Point out every malaria parasite and every leukocyte.
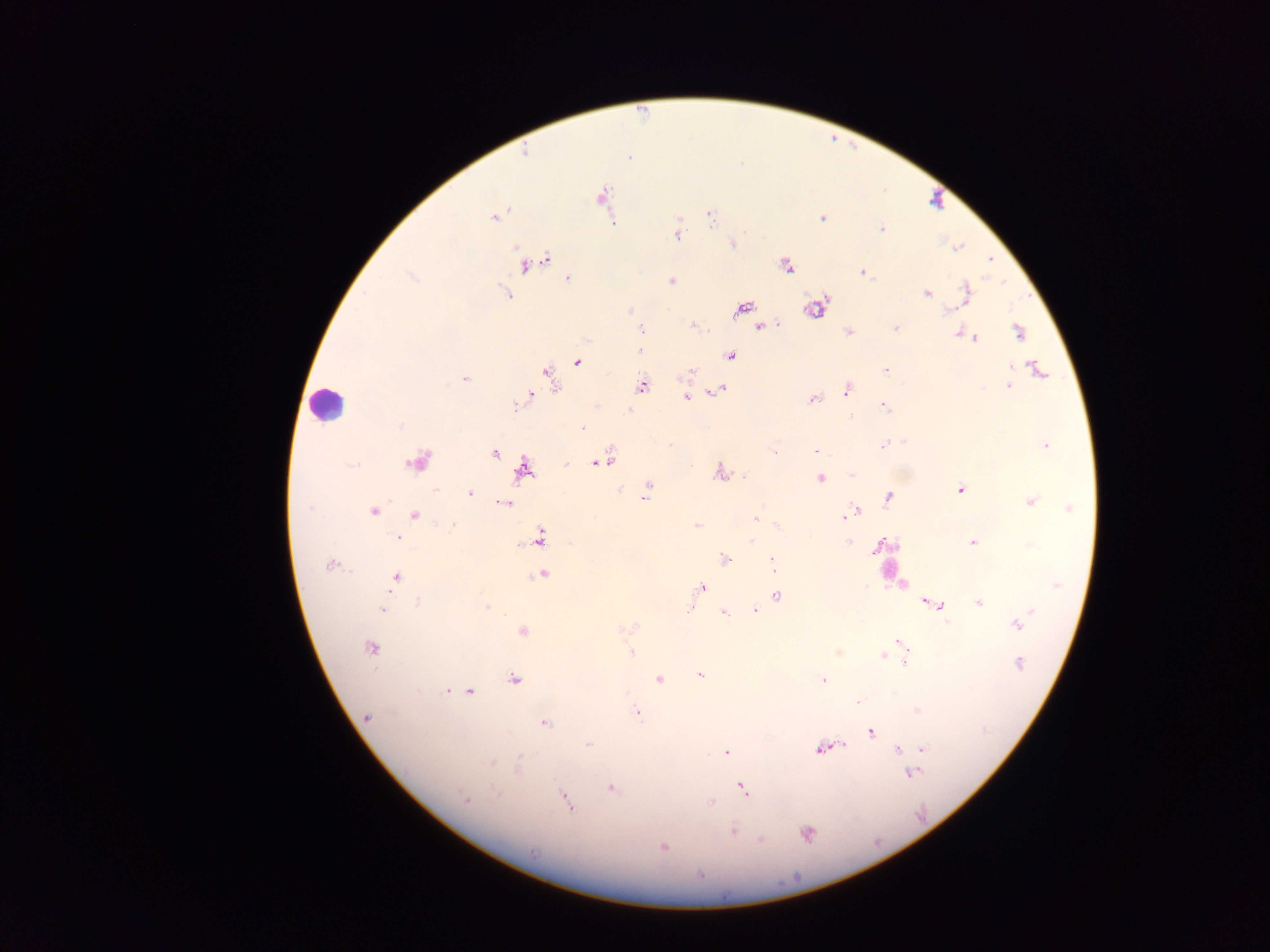

Approximate centers as (x, y) in pixels.
Malaria parasites: (629, 157), (602, 198), (494, 216), (710, 216), (822, 218), (613, 222), (882, 228), (677, 233), (732, 244), (959, 246), (991, 259), (533, 262), (786, 266), (863, 273), (410, 275), (568, 279), (671, 280), (967, 293), (507, 294), (927, 294), (815, 308), (742, 309), (629, 310), (950, 311), (693, 326), (760, 327), (896, 328), (641, 329), (848, 332), (1018, 332), (958, 334), (975, 338), (640, 350), (730, 356), (578, 362), (1037, 368), (885, 370), (690, 372), (548, 375), (464, 379), (641, 386), (1008, 386), (720, 389), (847, 389), (527, 397), (686, 397), (813, 399), (519, 403), (884, 405), (630, 411), (400, 426), (583, 428), (669, 445), (882, 445), (1046, 446), (816, 450), (495, 453), (775, 453), (417, 462), (601, 462), (566, 464), (524, 470), (719, 472), (744, 476), (851, 476), (821, 478), (649, 486), (960, 490), (470, 493), (646, 497), (889, 497), (1030, 502), (505, 503), (309, 507), (1069, 509), (374, 512), (858, 512), (851, 515), (415, 516), (844, 517), (755, 518), (453, 524), (777, 524), (697, 526), (398, 538), (540, 538), (752, 540), (849, 541), (972, 542), (882, 545), (725, 559), (772, 564), (330, 565), (542, 574), (396, 577), (1056, 586), (702, 587), (776, 596), (418, 602), (929, 603), (979, 603), (940, 604), (759, 606), (487, 607), (691, 608), (382, 610), (1032, 610), (755, 611), (724, 613), (946, 620), (1016, 625), (521, 631), (899, 642), (370, 647), (838, 652), (631, 654), (883, 655), (905, 662), (1020, 664), (699, 675), (513, 679), (659, 679), (823, 680), (447, 691), (470, 691), (858, 702), (636, 713), (367, 717), (545, 723), (871, 732), (588, 745), (843, 746), (820, 749), (923, 749), (898, 750), (726, 753), (521, 755), (492, 763), (517, 770), (912, 774), (612, 788), (743, 789), (497, 793), (465, 799), (567, 802), (711, 802), (732, 832), (807, 834), (760, 840), (664, 848), (534, 853).
Leukocytes: (327, 403), (892, 566).

Summary:
  - Field of view: single
  - Country: Ghana
  - Capture: mobile-phone photograph through a microscope
  - Image size: 1270×952 pixels
  - Preparation: thick blood smear